Identify the parasite.
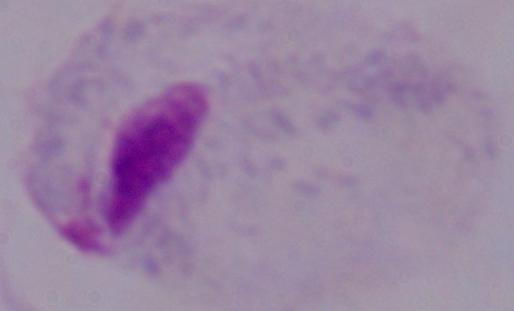
A trichomonad.

modality: photomicrograph
magnification: 1000x